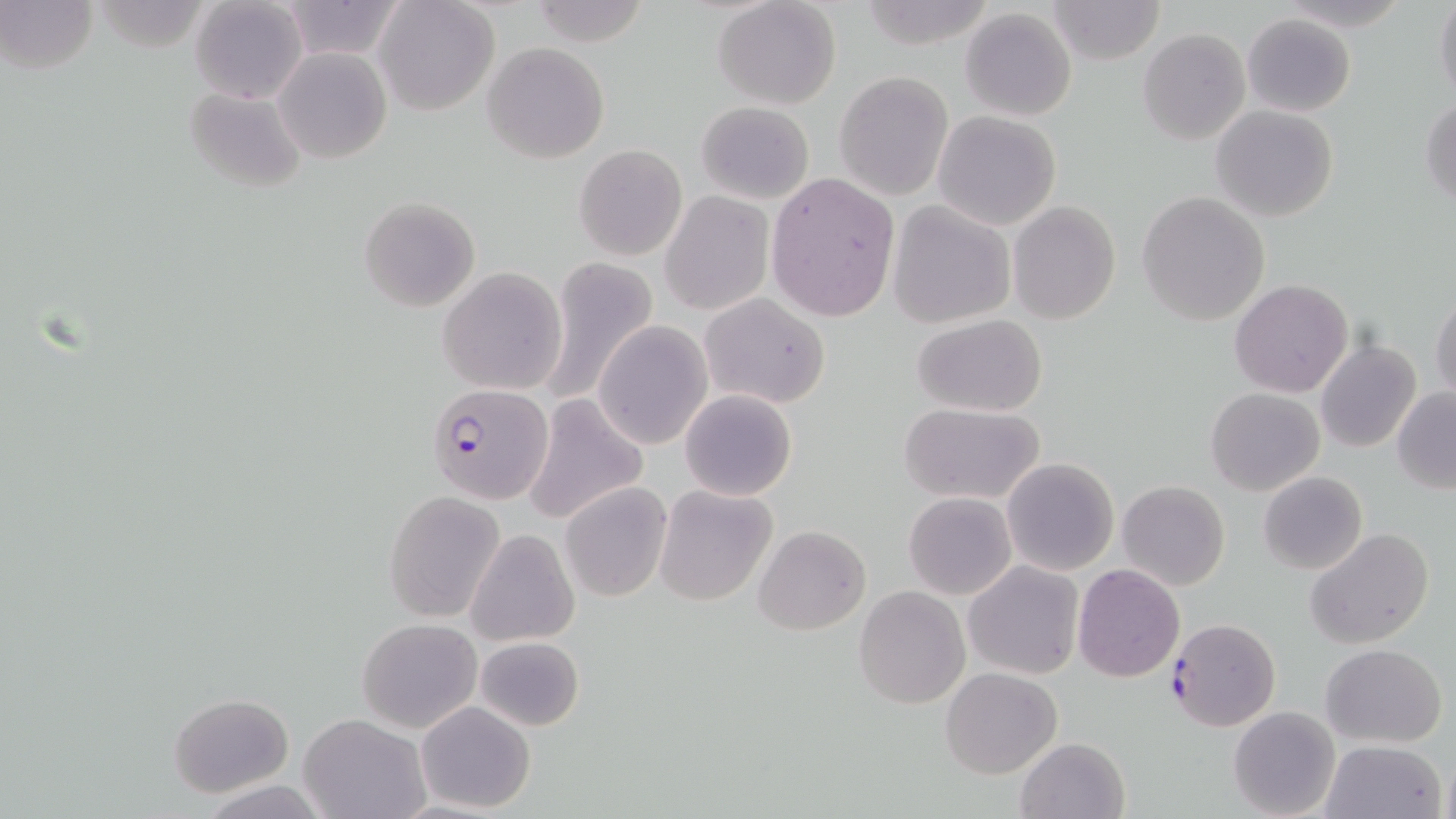

Approximate bounding boxes as named x1/y1/x2/y2 corners in pixels. Plasmodium falciparum-infected red blood cell locations: (x1=426, y1=382, x2=554, y2=503), (x1=1167, y1=618, x2=1280, y2=731). Uninfected red blood cell locations: (x1=1, y1=0, x2=98, y2=75), (x1=277, y1=0, x2=408, y2=61), (x1=375, y1=0, x2=499, y2=117), (x1=528, y1=0, x2=653, y2=47), (x1=713, y1=0, x2=840, y2=109), (x1=1045, y1=0, x2=1165, y2=64), (x1=1434, y1=0, x2=1456, y2=107), (x1=190, y1=1, x2=307, y2=103), (x1=960, y1=8, x2=1077, y2=121), (x1=1243, y1=13, x2=1356, y2=116), (x1=1138, y1=29, x2=1251, y2=144), (x1=482, y1=42, x2=610, y2=163), (x1=275, y1=47, x2=393, y2=163), (x1=835, y1=71, x2=951, y2=199), (x1=182, y1=86, x2=307, y2=195), (x1=1421, y1=98, x2=1455, y2=206), (x1=696, y1=101, x2=815, y2=203), (x1=1212, y1=106, x2=1338, y2=223), (x1=932, y1=110, x2=1061, y2=231), (x1=574, y1=144, x2=686, y2=261), (x1=763, y1=172, x2=900, y2=324), (x1=1138, y1=191, x2=1270, y2=326), (x1=660, y1=192, x2=774, y2=315), (x1=359, y1=197, x2=480, y2=312), (x1=887, y1=201, x2=1016, y2=328), (x1=1009, y1=201, x2=1121, y2=324), (x1=540, y1=257, x2=658, y2=405), (x1=437, y1=267, x2=567, y2=395), (x1=1230, y1=279, x2=1354, y2=397), (x1=1429, y1=289, x2=1456, y2=405), (x1=699, y1=293, x2=831, y2=409), (x1=912, y1=315, x2=1047, y2=417), (x1=593, y1=322, x2=713, y2=449), (x1=1316, y1=339, x2=1422, y2=453), (x1=1206, y1=387, x2=1324, y2=496), (x1=1392, y1=388, x2=1456, y2=493), (x1=679, y1=389, x2=798, y2=501), (x1=522, y1=394, x2=650, y2=527), (x1=899, y1=403, x2=1045, y2=505), (x1=1002, y1=457, x2=1119, y2=574), (x1=1259, y1=471, x2=1367, y2=575), (x1=1117, y1=480, x2=1229, y2=591), (x1=559, y1=481, x2=673, y2=602), (x1=653, y1=484, x2=777, y2=604), (x1=383, y1=490, x2=505, y2=622), (x1=904, y1=491, x2=1016, y2=599), (x1=753, y1=524, x2=870, y2=634), (x1=1305, y1=528, x2=1434, y2=649), (x1=466, y1=529, x2=578, y2=646), (x1=964, y1=560, x2=1083, y2=679), (x1=1072, y1=564, x2=1186, y2=683), (x1=853, y1=585, x2=971, y2=709), (x1=358, y1=618, x2=482, y2=733), (x1=474, y1=636, x2=584, y2=731), (x1=1320, y1=644, x2=1447, y2=747), (x1=940, y1=666, x2=1064, y2=779), (x1=169, y1=691, x2=293, y2=797), (x1=416, y1=701, x2=536, y2=814), (x1=1227, y1=704, x2=1341, y2=818), (x1=302, y1=714, x2=431, y2=819), (x1=1014, y1=737, x2=1130, y2=819), (x1=1319, y1=739, x2=1448, y2=819). Slide-level diagnosis: Plasmodium falciparum. Optical microscopy. 1000x magnification. May-Grünwald-Giemsa stain. Image is 1456×819 pixels. Thin blood film. One field of a larger specimen.